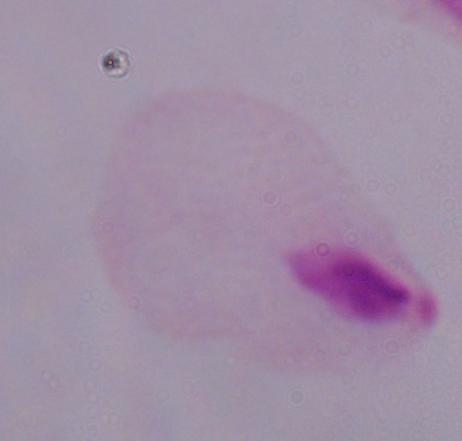
Summary:
  - Magnification: 1000x
  - Modality: micrograph
  - Identification: trichomonad